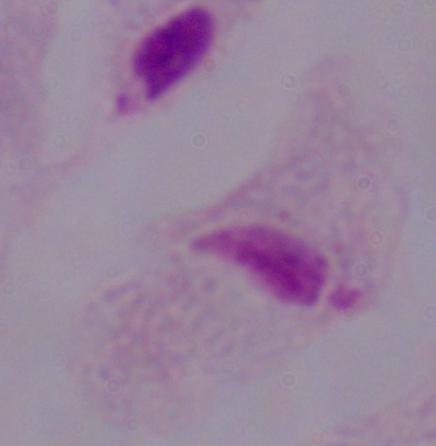

Summary:
  - Magnification: 1000x
  - Identification: trichomonad
  - Modality: photomicrograph